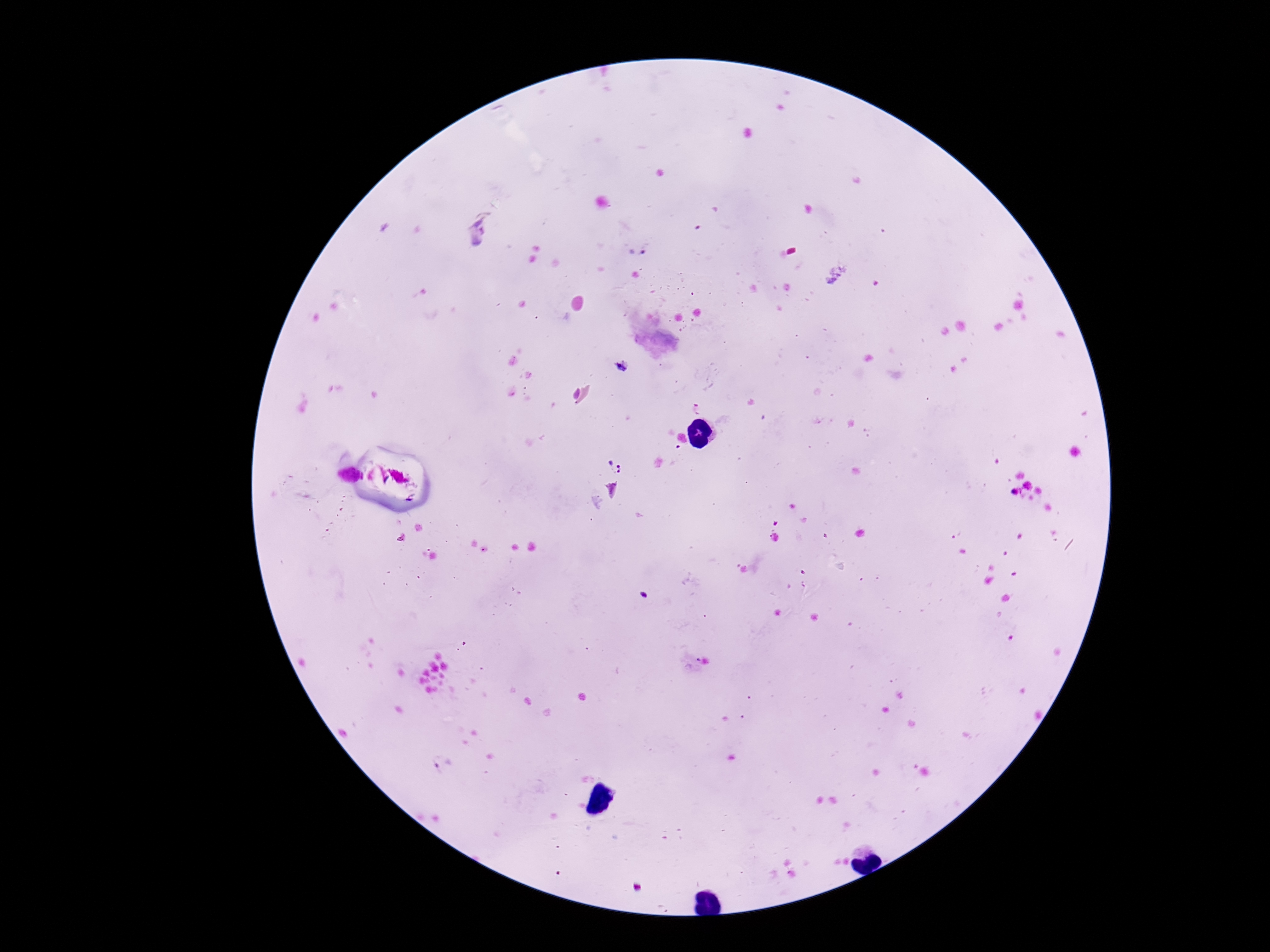

Plasmodium parasite locations = approximate centers as [x, y] in pixels: [612, 465]
capture = smartphone camera through the microscope eyepiece
field of view = single
stain = Giemsa
patient malaria status = positive
preparation = thick blood smear
magnification = 100x
image size = 1270×952 pixels